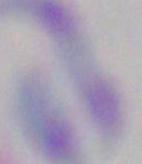
identification: Toxoplasma gondii
magnification: 1000x
modality: photomicrograph